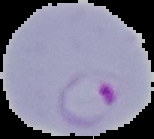

Cell region segmented out of the field of view; the surrounding area is masked to black. Result: malaria parasites detected. From a thin blood film. Image is 154×139 pixels.